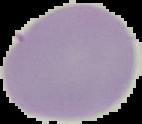
preparation: thin blood film
malaria_status: uninfected
image_type: segmented cell region with the area outside set to black
image_size: 142×124 pixels